Locate every P. falciparum parasite and identify its life-cycle stage.
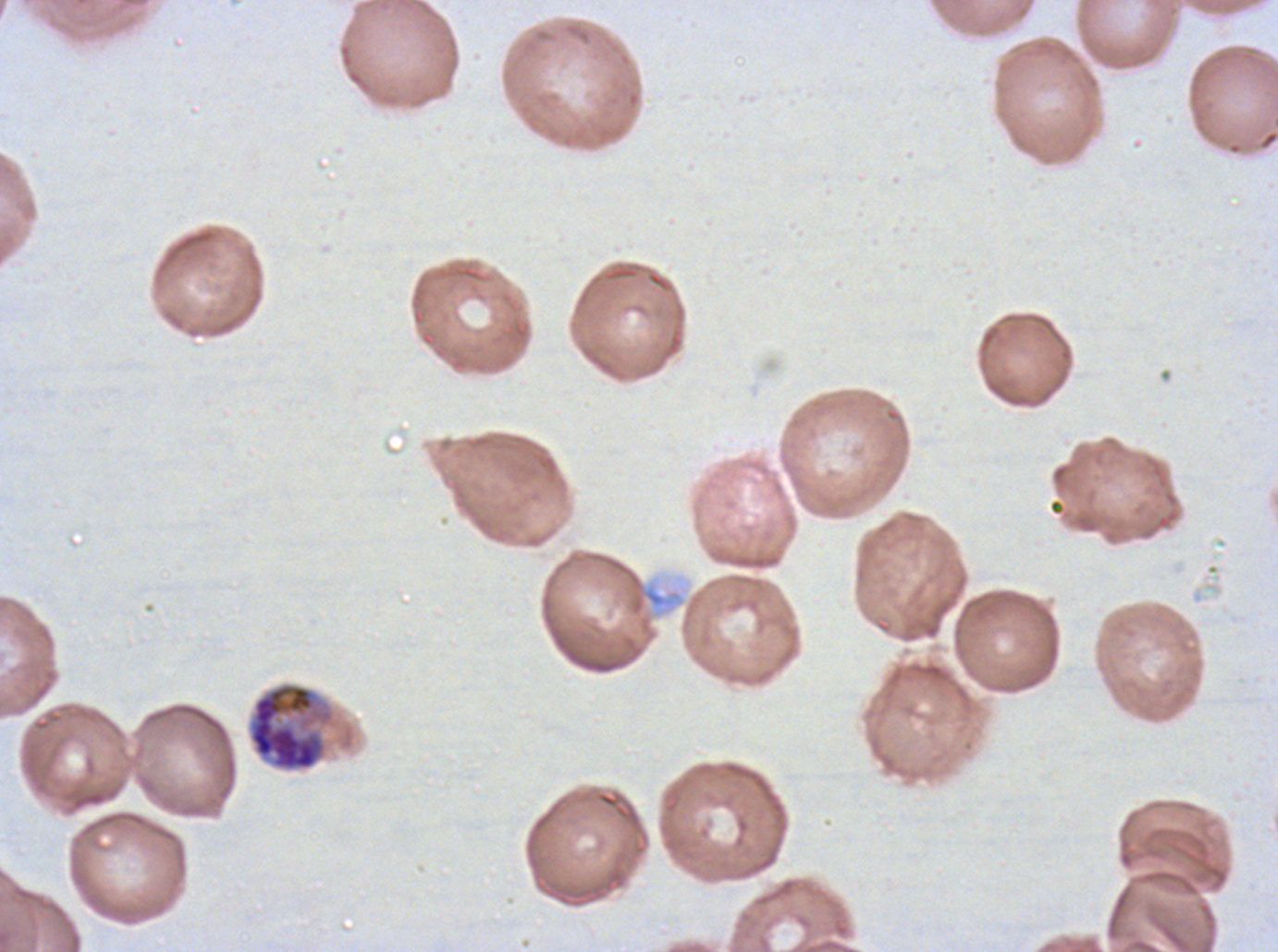

Approximate bounding boxes as [x1, y1, x2, y2] in pixels.
Early schizonts: [246, 681, 341, 774].
No rings, late-ring/early-trophozoite forms, mid trophozoites, late trophozoites, late schizonts, segmenters, or gametocytes observed.

A sub-image separated from a larger composite. Giemsa stain. P. falciparum cultured ex vivo for 24 to 48 hours, from a patient in The Gambia. Thin blood smear. Image is 1278×952 pixels.